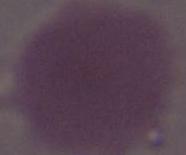

identification: red blood cell
magnification: 1000x
modality: micrograph